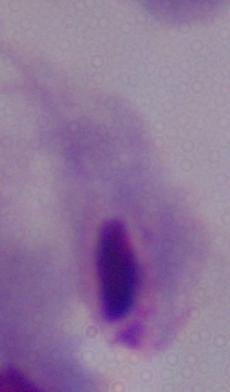 A trichomonad is shown. Micrograph. Captured at 1000x magnification.